Give the extent of all Plasmodium falciparum-infected red blood cells.
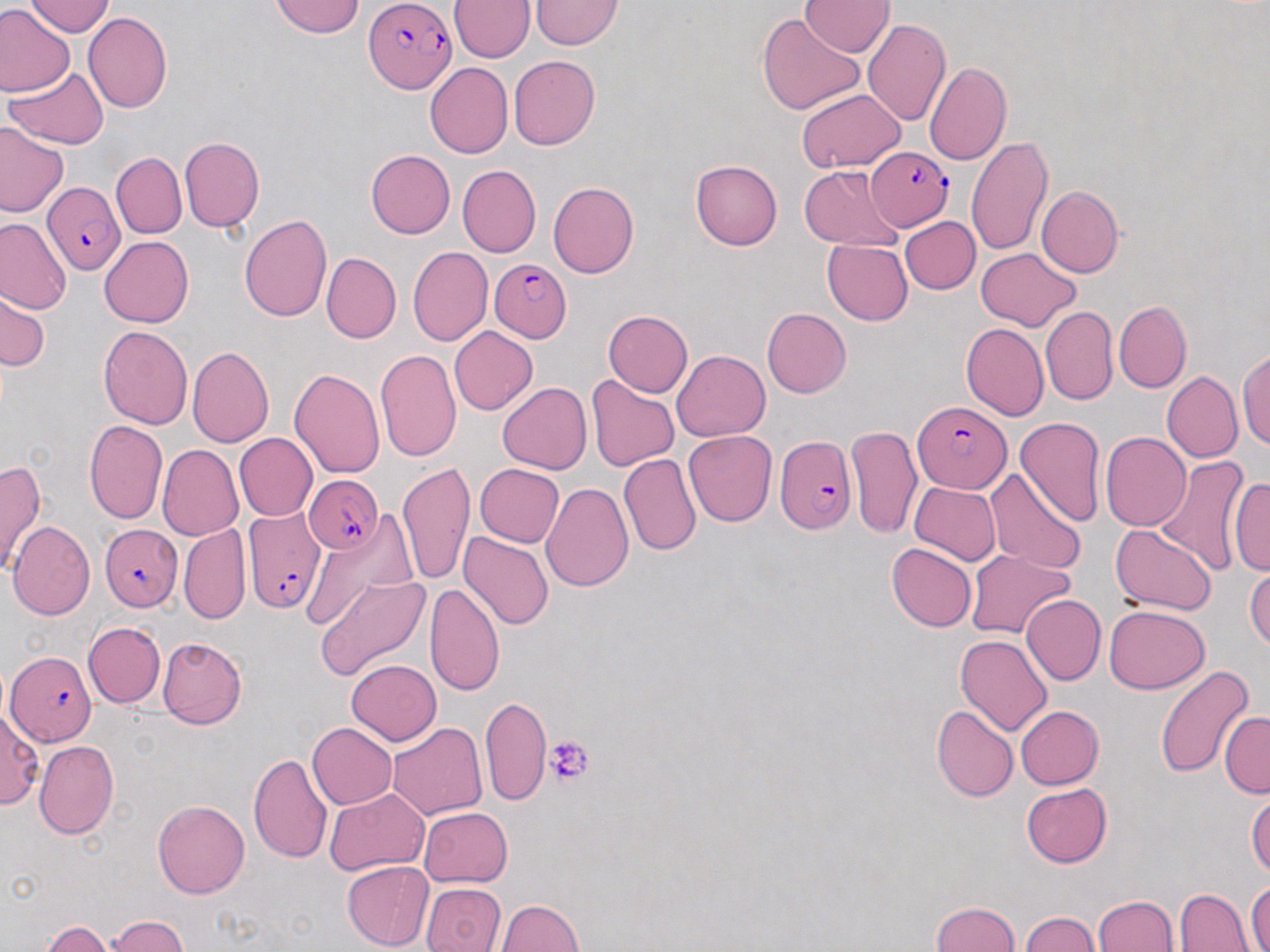
Approximate bounding boxes as (x1,y1)-(x2,y2) corner pairs in pixels.
Plasmodium falciparum-infected red blood cells: (365,0)-(455,93), (866,146)-(952,232), (42,183)-(126,275), (488,258)-(571,342), (912,402)-(1012,494), (776,436)-(856,533), (305,474)-(383,552), (240,505)-(327,614), (102,523)-(183,610), (6,649)-(95,747).

Uninfected red blood cell locations: (25,0)-(115,37), (270,0)-(364,38), (449,0)-(535,63), (530,1)-(624,50), (799,1)-(894,56), (0,5)-(73,98), (82,11)-(173,115), (757,11)-(864,115), (862,18)-(952,126), (509,55)-(600,150), (924,61)-(1012,166), (425,62)-(512,159), (5,66)-(109,149), (796,89)-(904,171), (0,123)-(67,216), (179,137)-(264,233), (965,137)-(1053,257), (364,149)-(455,239), (111,152)-(186,239), (690,159)-(781,251), (456,165)-(541,258), (799,166)-(903,249), (548,181)-(639,277), (1037,187)-(1124,278), (239,213)-(332,321), (900,216)-(981,293), (1,217)-(71,314), (100,236)-(194,328), (822,240)-(913,325), (407,246)-(493,346), (975,248)-(1080,331), (321,253)-(401,344), (1,288)-(51,372), (1114,300)-(1191,393), (1040,305)-(1117,405), (762,307)-(851,398), (602,310)-(693,397), (960,323)-(1049,420), (98,325)-(193,429), (448,326)-(539,415), (187,346)-(273,448), (375,349)-(461,462), (672,349)-(770,441), (1237,349)-(1270,450), (289,367)-(386,478), (1162,371)-(1243,463), (586,375)-(679,472), (497,382)-(592,474), (1014,417)-(1106,527), (84,420)-(166,525), (847,425)-(922,539), (683,430)-(777,527), (1101,431)-(1192,531), (234,433)-(317,521), (157,444)-(242,541), (1152,452)-(1251,577), (618,453)-(702,555), (0,459)-(45,575), (398,462)-(475,589), (570,462)-(679,598), (475,463)-(564,547), (985,467)-(1088,576), (1228,475)-(1269,575), (911,481)-(1000,564), (541,483)-(634,592), (301,516)-(415,633), (8,520)-(96,620), (179,523)-(251,625), (1109,524)-(1216,614), (458,531)-(553,630), (887,543)-(976,632), (965,549)-(1074,639), (1245,561)-(1269,654), (315,575)-(431,683), (424,582)-(505,696), (1022,593)-(1107,686), (1105,605)-(1210,694), (83,621)-(164,708), (955,634)-(1054,737), (157,637)-(247,730), (345,658)-(441,745), (1153,664)-(1254,779), (479,695)-(551,805), (930,703)-(1018,802), (1015,705)-(1103,789), (1,708)-(45,808), (1219,712)-(1270,798), (307,722)-(397,810), (388,722)-(487,821), (33,741)-(119,839), (248,754)-(334,864), (1021,783)-(1113,867), (1247,786)-(1269,881), (323,788)-(429,876), (153,801)-(250,899), (418,806)-(513,887), (341,861)-(435,951), (1247,878)-(1270,952), (421,882)-(507,952), (1174,888)-(1255,952), (1092,895)-(1179,952), (496,898)-(583,951), (929,902)-(1022,952), (1019,912)-(1104,952), (105,915)-(189,951), (41,922)-(113,952). Platelet locations: (544,736)-(593,787). Slide-level diagnosis: Plasmodium falciparum. Single field of view. 1000x magnification. Optical microscopy. Thin blood smear. May-Grünwald-Giemsa stain. Image is 1270×952 pixels.